Report the malaria status.
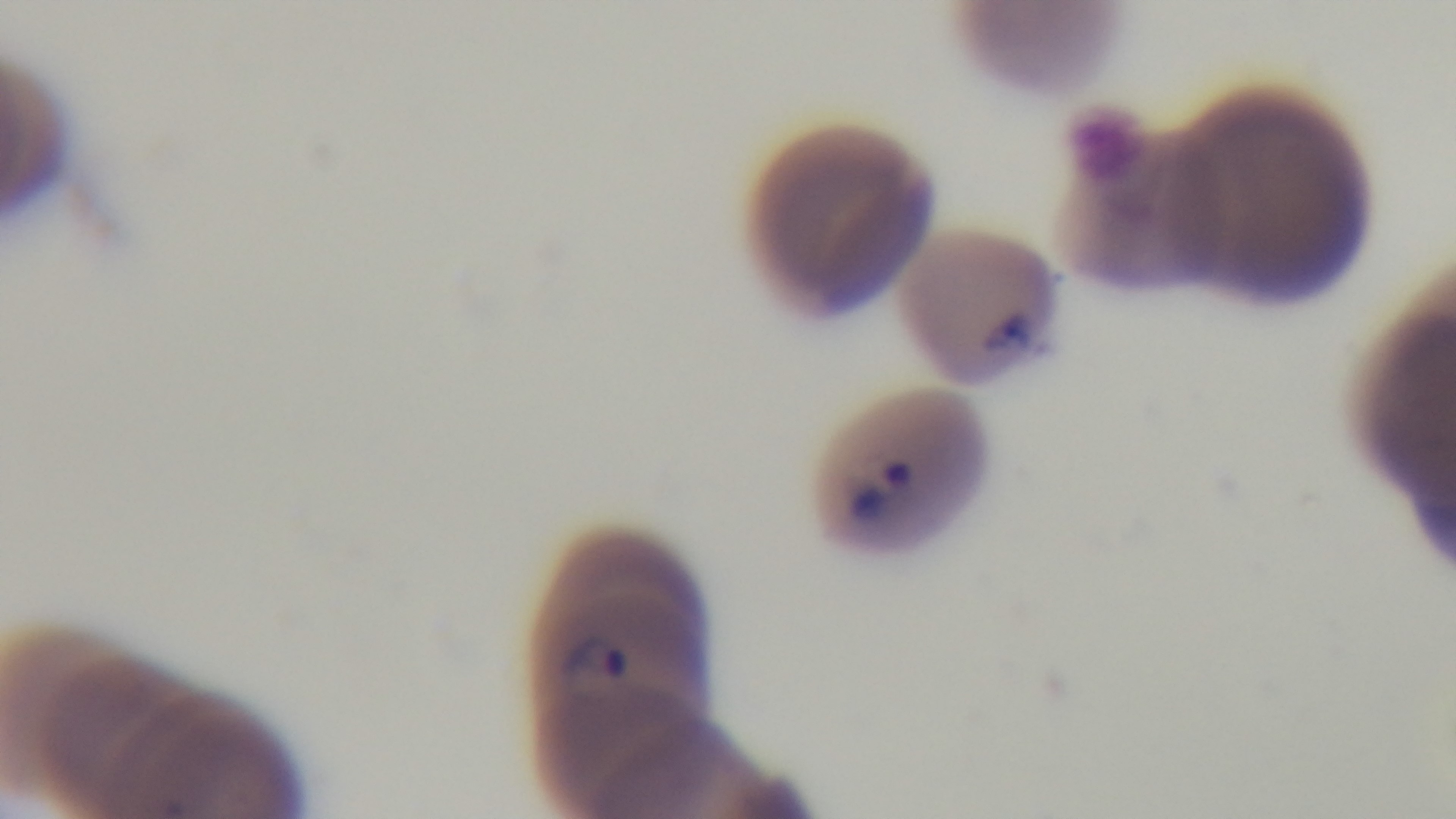
It is infected.

stain: Giemsa
objective: 100x oil immersion
capture: mounted 4K digital camera
field_of_view: one from the slide
preparation: thin smear
modality: light microscopy